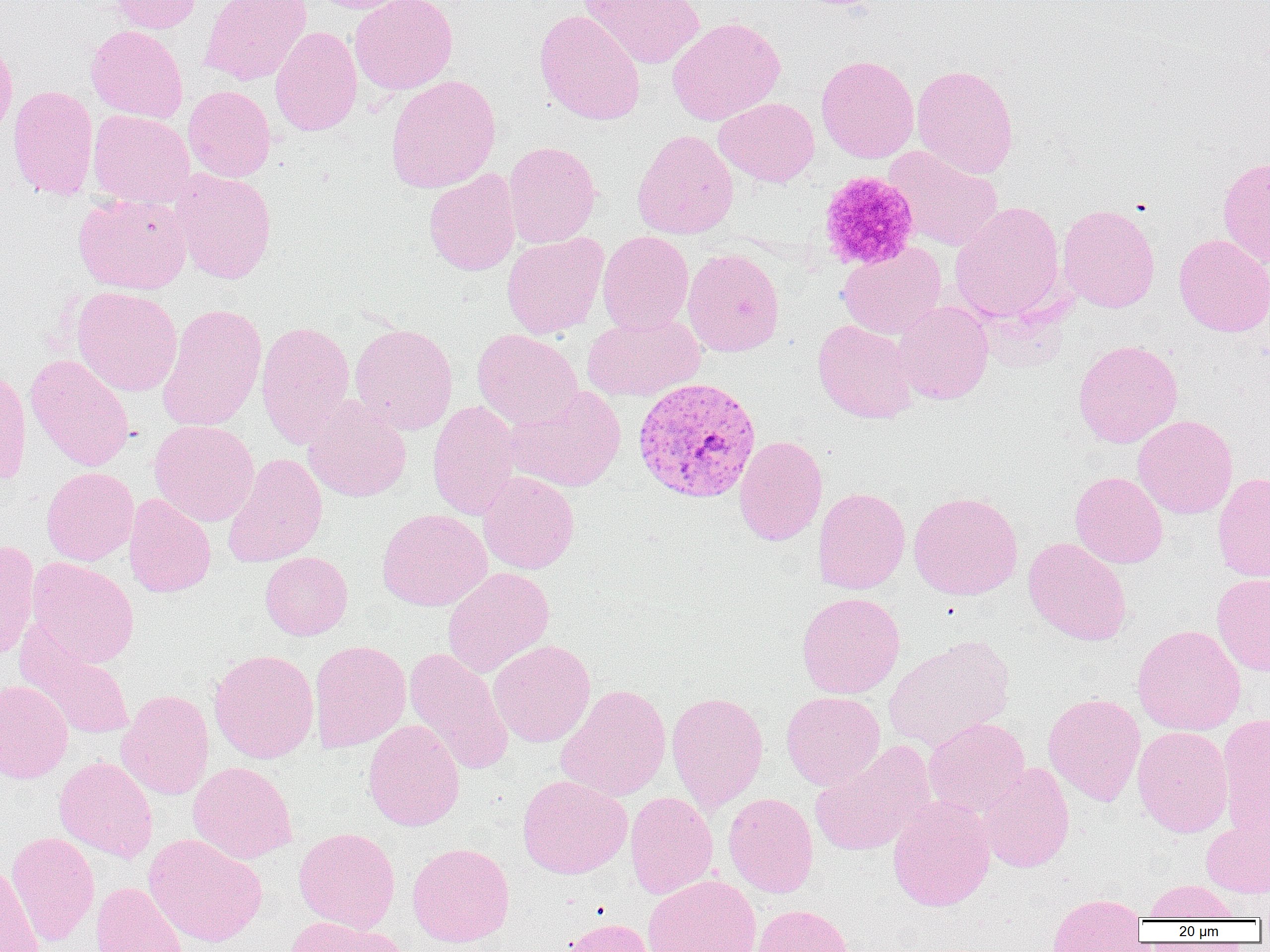
Summary:
  - Coordinate format: approximate bounding boxes as named x1/y1/x2/y2 corners in pixels
  - Uninfected red blood cell locations: (x1=109, y1=0, x2=202, y2=34), (x1=200, y1=0, x2=312, y2=85), (x1=311, y1=0, x2=413, y2=13), (x1=350, y1=0, x2=458, y2=94), (x1=579, y1=0, x2=705, y2=69), (x1=534, y1=9, x2=646, y2=125), (x1=667, y1=17, x2=785, y2=126), (x1=86, y1=24, x2=188, y2=123), (x1=270, y1=26, x2=363, y2=136), (x1=0, y1=35, x2=17, y2=144), (x1=816, y1=55, x2=919, y2=163), (x1=912, y1=64, x2=1018, y2=179), (x1=385, y1=74, x2=501, y2=193), (x1=7, y1=84, x2=98, y2=198), (x1=183, y1=86, x2=276, y2=182), (x1=714, y1=97, x2=820, y2=187), (x1=88, y1=110, x2=194, y2=208), (x1=631, y1=129, x2=738, y2=240), (x1=502, y1=141, x2=601, y2=248), (x1=884, y1=146, x2=1004, y2=252), (x1=1218, y1=156, x2=1270, y2=267), (x1=169, y1=168, x2=278, y2=284), (x1=424, y1=169, x2=521, y2=276), (x1=73, y1=193, x2=192, y2=294), (x1=950, y1=201, x2=1066, y2=322), (x1=1058, y1=204, x2=1160, y2=313), (x1=597, y1=231, x2=694, y2=334), (x1=502, y1=232, x2=609, y2=339), (x1=1174, y1=234, x2=1270, y2=337), (x1=837, y1=242, x2=946, y2=339), (x1=682, y1=248, x2=784, y2=357), (x1=71, y1=286, x2=182, y2=396), (x1=892, y1=300, x2=994, y2=405), (x1=157, y1=303, x2=267, y2=432), (x1=582, y1=313, x2=705, y2=402), (x1=813, y1=318, x2=919, y2=424), (x1=256, y1=321, x2=355, y2=448), (x1=350, y1=323, x2=458, y2=434), (x1=472, y1=328, x2=583, y2=428), (x1=1072, y1=339, x2=1183, y2=448), (x1=25, y1=354, x2=135, y2=471), (x1=0, y1=367, x2=31, y2=485), (x1=504, y1=386, x2=626, y2=492), (x1=303, y1=396, x2=411, y2=503), (x1=428, y1=400, x2=522, y2=520), (x1=1133, y1=415, x2=1237, y2=520), (x1=149, y1=420, x2=259, y2=527), (x1=734, y1=435, x2=827, y2=546), (x1=222, y1=452, x2=327, y2=568), (x1=41, y1=467, x2=138, y2=565), (x1=478, y1=471, x2=580, y2=574), (x1=1069, y1=471, x2=1168, y2=569), (x1=1212, y1=471, x2=1270, y2=583), (x1=813, y1=487, x2=910, y2=594), (x1=908, y1=491, x2=1023, y2=600), (x1=123, y1=494, x2=216, y2=598), (x1=377, y1=508, x2=492, y2=611), (x1=1023, y1=537, x2=1131, y2=646), (x1=0, y1=540, x2=41, y2=663), (x1=260, y1=551, x2=353, y2=640), (x1=26, y1=557, x2=139, y2=668), (x1=442, y1=566, x2=555, y2=678), (x1=1211, y1=572, x2=1270, y2=677), (x1=796, y1=591, x2=905, y2=699), (x1=15, y1=621, x2=135, y2=741), (x1=1132, y1=624, x2=1246, y2=735), (x1=883, y1=637, x2=1015, y2=751), (x1=309, y1=639, x2=411, y2=753), (x1=488, y1=640, x2=595, y2=747), (x1=404, y1=647, x2=514, y2=776), (x1=209, y1=649, x2=319, y2=763), (x1=0, y1=679, x2=73, y2=784), (x1=556, y1=684, x2=671, y2=802), (x1=116, y1=689, x2=214, y2=800), (x1=781, y1=690, x2=885, y2=790), (x1=666, y1=692, x2=768, y2=812), (x1=1042, y1=693, x2=1146, y2=806), (x1=1217, y1=713, x2=1270, y2=835), (x1=923, y1=717, x2=1031, y2=819), (x1=363, y1=720, x2=465, y2=831), (x1=1132, y1=725, x2=1233, y2=837), (x1=809, y1=742, x2=934, y2=858), (x1=53, y1=756, x2=158, y2=862), (x1=187, y1=761, x2=298, y2=864), (x1=977, y1=762, x2=1075, y2=873), (x1=517, y1=775, x2=632, y2=878), (x1=625, y1=791, x2=718, y2=899), (x1=723, y1=792, x2=819, y2=897), (x1=888, y1=795, x2=996, y2=912), (x1=1201, y1=809, x2=1270, y2=899), (x1=294, y1=827, x2=400, y2=932), (x1=5, y1=831, x2=100, y2=947), (x1=143, y1=833, x2=267, y2=947), (x1=407, y1=842, x2=515, y2=948), (x1=0, y1=863, x2=44, y2=952), (x1=642, y1=874, x2=761, y2=952), (x1=1143, y1=880, x2=1240, y2=922), (x1=91, y1=882, x2=189, y2=952), (x1=1046, y1=893, x2=1147, y2=952), (x1=751, y1=903, x2=854, y2=952), (x1=281, y1=916, x2=407, y2=952), (x1=561, y1=917, x2=656, y2=952)
  - Plasmodium vivax-infected red blood cell locations: (x1=632, y1=376, x2=762, y2=503)
  - Platelet locations: (x1=817, y1=170, x2=920, y2=271)
  - Slide-level diagnosis: Plasmodium vivax
  - Magnification: 1000x
  - Preparation: thin blood film
  - Image size: 1270×952 pixels
  - Modality: optical microscopy
  - Field of view: single